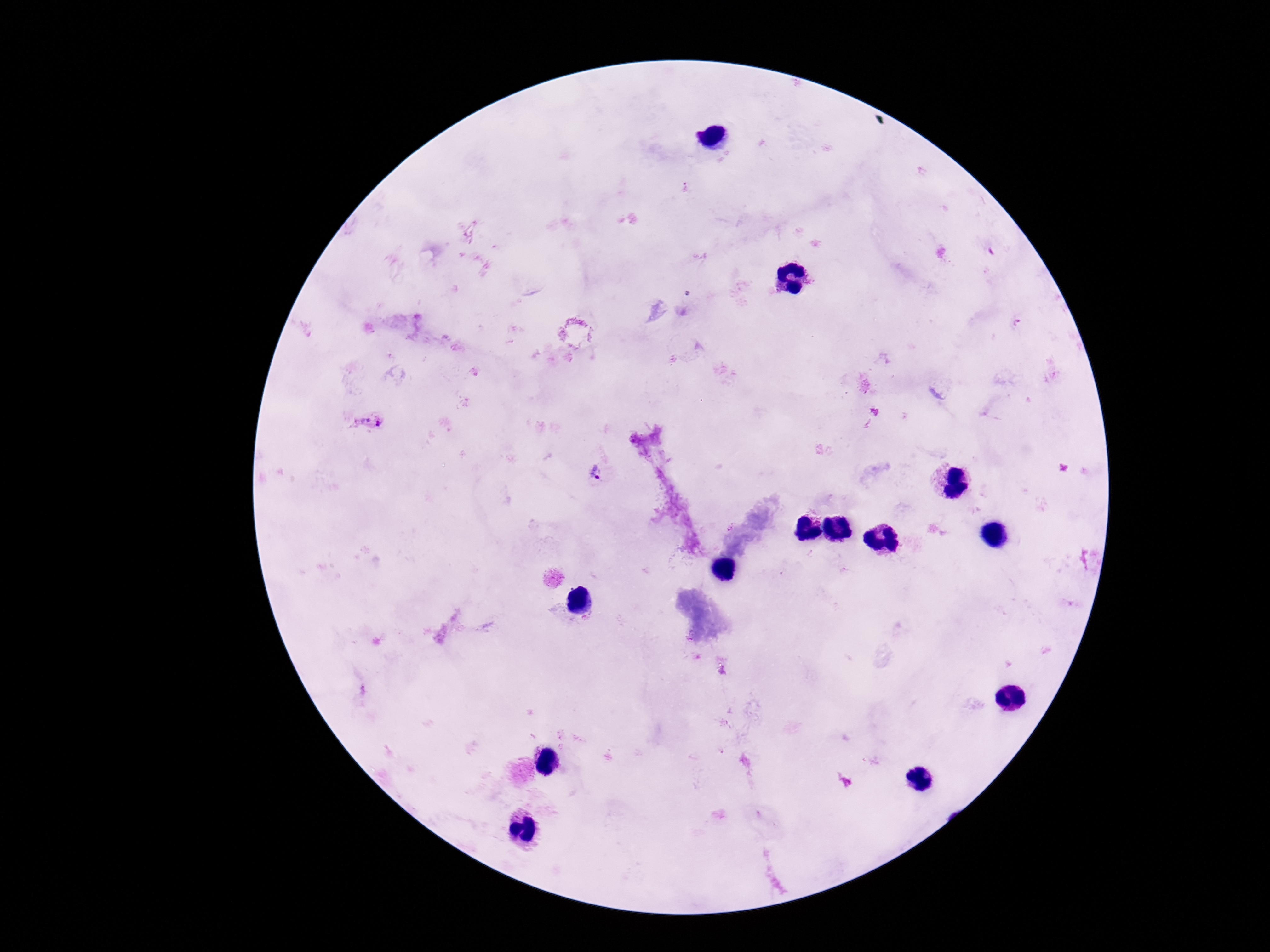
Approximate centers as {x, y} in pixels.
Summary:
  - Plasmodium parasite locations: {369, 421}, {596, 473}
  - Field of view: one from this slide
  - Image size: 1270×952 pixels
  - Preparation: thick blood film
  - Stain: Giemsa
  - Patient malaria status: infected
  - Capture: smartphone camera through the microscope eyepiece
  - Magnification: 100x